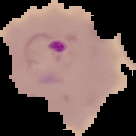

Malaria status: parasitized. From a thin blood smear. Image is 136×136 pixels. The area outside the segmented cell region is set to black.